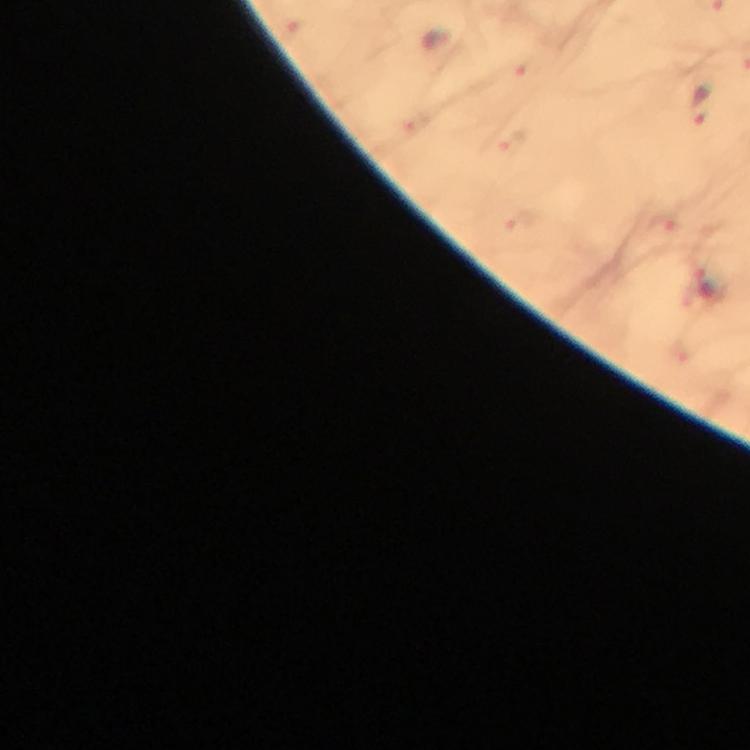
context = from a malaria diagnostic workup
cropped from = one field of view
malaria parasite locations = approximate centers as (x, y) in pixels: (527, 67), (703, 105), (511, 143), (521, 223), (663, 226), (705, 281)
capture = smartphone mounted on the microscope
preparation = thick blood film
magnification = 100x
image size = 750×750 pixels
stain = Giemsa
immersion oil = used